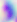
Summary:
  - Magnification: 400x
  - Modality: photomicrograph
  - Identification: Toxoplasma gondii